Give the position of every malaria parasite, noting whether each is a trophozoite, schizont, or gametocyte.
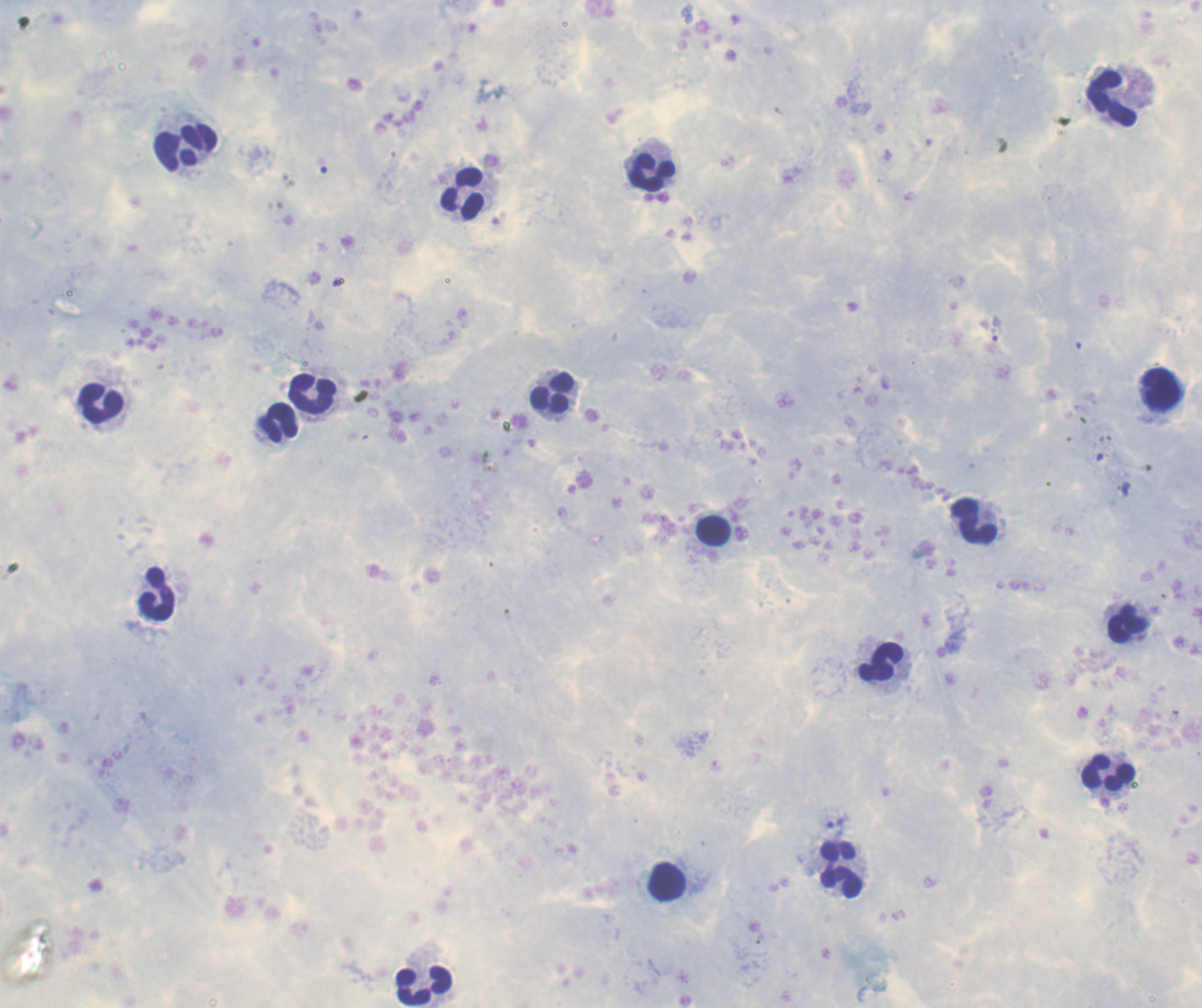

Approximate centers as (x, y) in pixels.
Trophozoites: (837, 824).
No schizont or gametocyte forms observed.

Approximate centers as (x, y) in pixels. Leukocyte locations: (1114, 97), (186, 147), (651, 173), (464, 192), (1160, 390), (551, 393), (314, 396), (102, 403), (279, 422), (972, 520), (714, 531), (156, 593), (1126, 623), (881, 660), (1109, 772), (843, 870), (666, 882), (424, 985). Romanowsky stain. Single field of view. Background quality: poor. 100x magnification. Thick blood smear. Previously used in a real diagnosis. Image is 1202×1008 pixels.